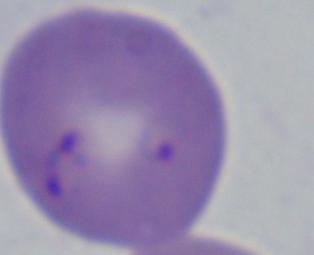

modality = photomicrograph
magnification = 1000x
identification = Babesia